Comment on the morphology of the red blood cells.
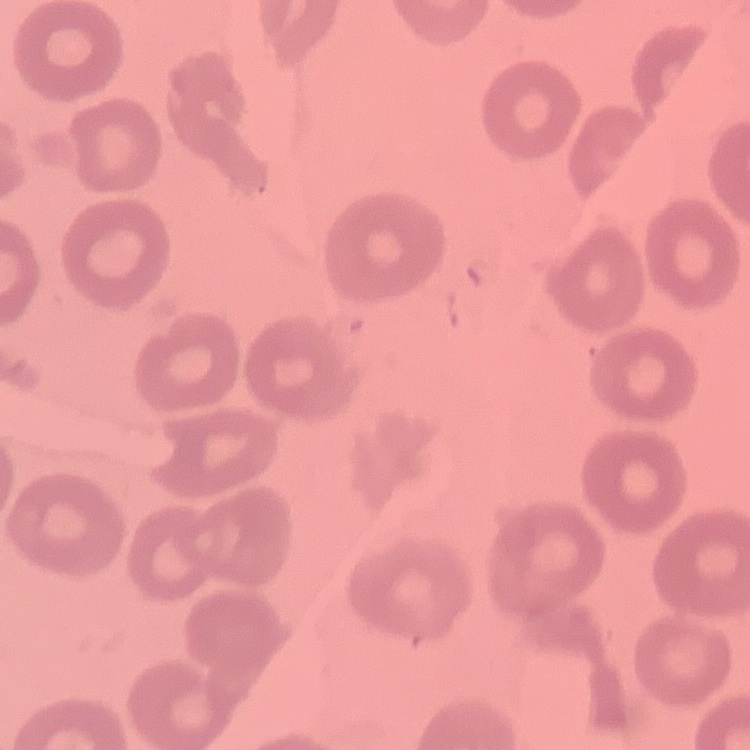

They show no rouleaux formation.

stain = Field's or Giemsa
preparation = thin peripheral smear
image type = one tile cut from a larger photomicrograph